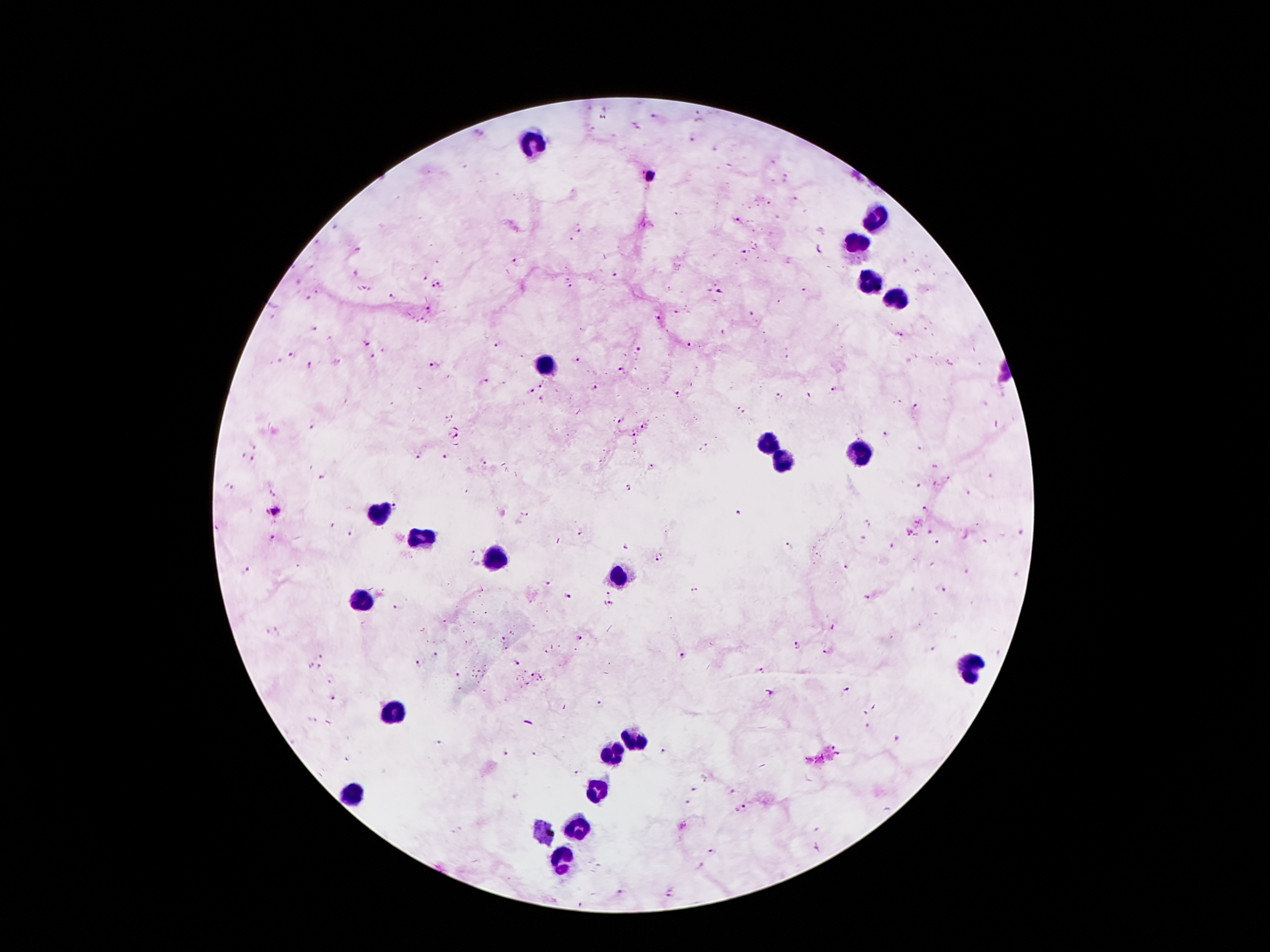

Approximate object centers, in pixels from the top-left corner. Leukocyte locations: (x=535, y=143), (x=877, y=219), (x=858, y=243), (x=866, y=277), (x=898, y=305), (x=546, y=366), (x=772, y=448), (x=861, y=451), (x=784, y=462), (x=383, y=511), (x=420, y=536), (x=494, y=560), (x=619, y=578), (x=362, y=599), (x=968, y=669), (x=389, y=712), (x=632, y=740), (x=614, y=754), (x=601, y=789), (x=352, y=791), (x=580, y=828), (x=561, y=857). Malaria parasite locations: (x=653, y=116), (x=694, y=140), (x=739, y=217), (x=577, y=231), (x=572, y=238), (x=744, y=252), (x=516, y=262), (x=612, y=275), (x=422, y=277), (x=441, y=285), (x=431, y=286), (x=572, y=288), (x=805, y=288), (x=718, y=291), (x=392, y=296), (x=310, y=298), (x=428, y=309), (x=677, y=312), (x=752, y=313), (x=659, y=316), (x=315, y=328), (x=722, y=332), (x=901, y=335), (x=370, y=343), (x=692, y=344), (x=496, y=345), (x=637, y=348), (x=291, y=353), (x=372, y=358), (x=577, y=359), (x=310, y=364), (x=434, y=365), (x=620, y=368), (x=483, y=383), (x=543, y=385), (x=595, y=387), (x=834, y=388), (x=532, y=391), (x=677, y=393), (x=780, y=395), (x=810, y=396), (x=915, y=406), (x=621, y=419), (x=313, y=425), (x=644, y=425), (x=635, y=432), (x=887, y=434), (x=254, y=444), (x=704, y=448), (x=253, y=456), (x=417, y=456), (x=448, y=456), (x=483, y=461), (x=935, y=466), (x=650, y=467), (x=321, y=476), (x=935, y=483), (x=228, y=486), (x=920, y=486), (x=628, y=488), (x=968, y=493), (x=271, y=494), (x=925, y=506), (x=396, y=507), (x=276, y=511), (x=738, y=513), (x=524, y=515), (x=1019, y=530), (x=907, y=531), (x=929, y=531), (x=352, y=533), (x=580, y=533), (x=273, y=536), (x=865, y=539), (x=983, y=541), (x=936, y=542), (x=790, y=546), (x=657, y=559), (x=846, y=566), (x=246, y=570), (x=549, y=584), (x=693, y=590), (x=944, y=590), (x=608, y=593), (x=567, y=595), (x=867, y=598), (x=612, y=605), (x=397, y=609), (x=501, y=636), (x=579, y=636), (x=797, y=646), (x=826, y=651), (x=435, y=654), (x=683, y=655), (x=320, y=656), (x=417, y=661), (x=516, y=663), (x=312, y=665), (x=320, y=666), (x=763, y=671), (x=458, y=676), (x=332, y=697), (x=600, y=702), (x=441, y=742), (x=663, y=750), (x=504, y=753), (x=533, y=753), (x=577, y=772), (x=693, y=789), (x=686, y=802), (x=743, y=807), (x=712, y=852), (x=621, y=893), (x=671, y=894). 100x magnification. Patient malaria status: positive for Plasmodium falciparum. Smartphone photograph taken through the microscope eyepiece. One field from this slide. Thick blood smear. Giemsa stain. Image is 1270×952 pixels.